Report the malaria status of this cell.
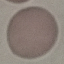

It is uninfected.

Thin blood film. Acquired by smartphone through the microscope eyepiece. Giemsa stain. Cell patch, automatically extracted from a larger field of view and resized to 64 × 64 pixels.